Report the malaria status of this cell.
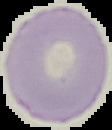
Uninfected.

preparation = thin blood smear
image size = 112×130 pixels
image type = segmented cell region with the area outside set to black